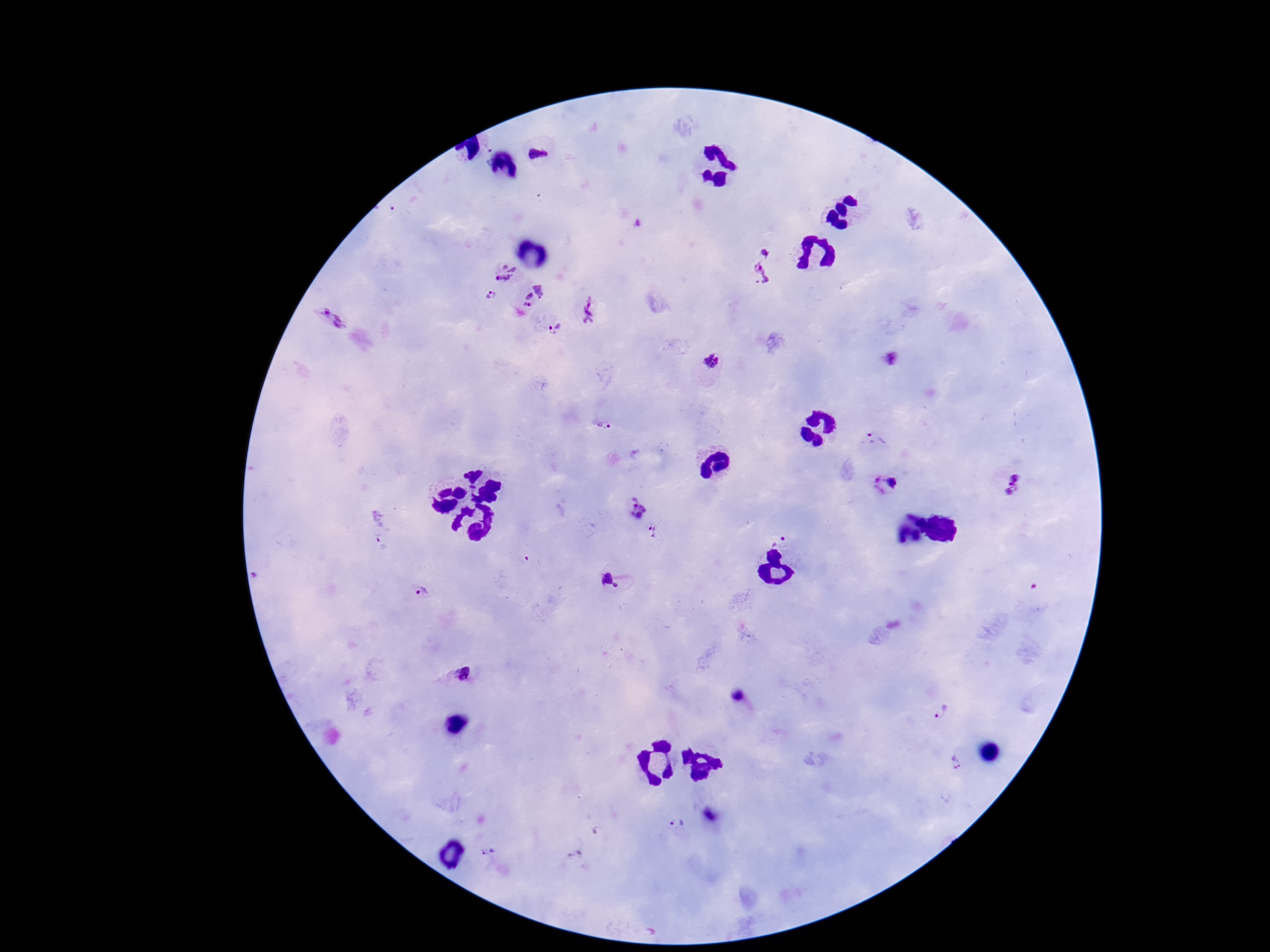
Approximate object centers, in pixels from the top-left corner.
Summary:
  - Plasmodium parasite locations: (x=540, y=154), (x=767, y=251), (x=504, y=272), (x=762, y=275), (x=491, y=295), (x=532, y=296), (x=590, y=308), (x=333, y=318), (x=553, y=328), (x=890, y=360), (x=710, y=365), (x=603, y=427), (x=877, y=441), (x=890, y=482), (x=1012, y=485), (x=636, y=508), (x=654, y=530), (x=780, y=536), (x=383, y=541), (x=534, y=562), (x=611, y=581), (x=420, y=591), (x=462, y=674), (x=941, y=712), (x=956, y=762), (x=678, y=824), (x=487, y=854)
  - Image size: 1270×952 pixels
  - Preparation: thick blood film
  - Capture: smartphone camera through the microscope eyepiece
  - Magnification: 100x
  - Field of view: one from this slide
  - Stain: Giemsa
  - Patient malaria status: positive